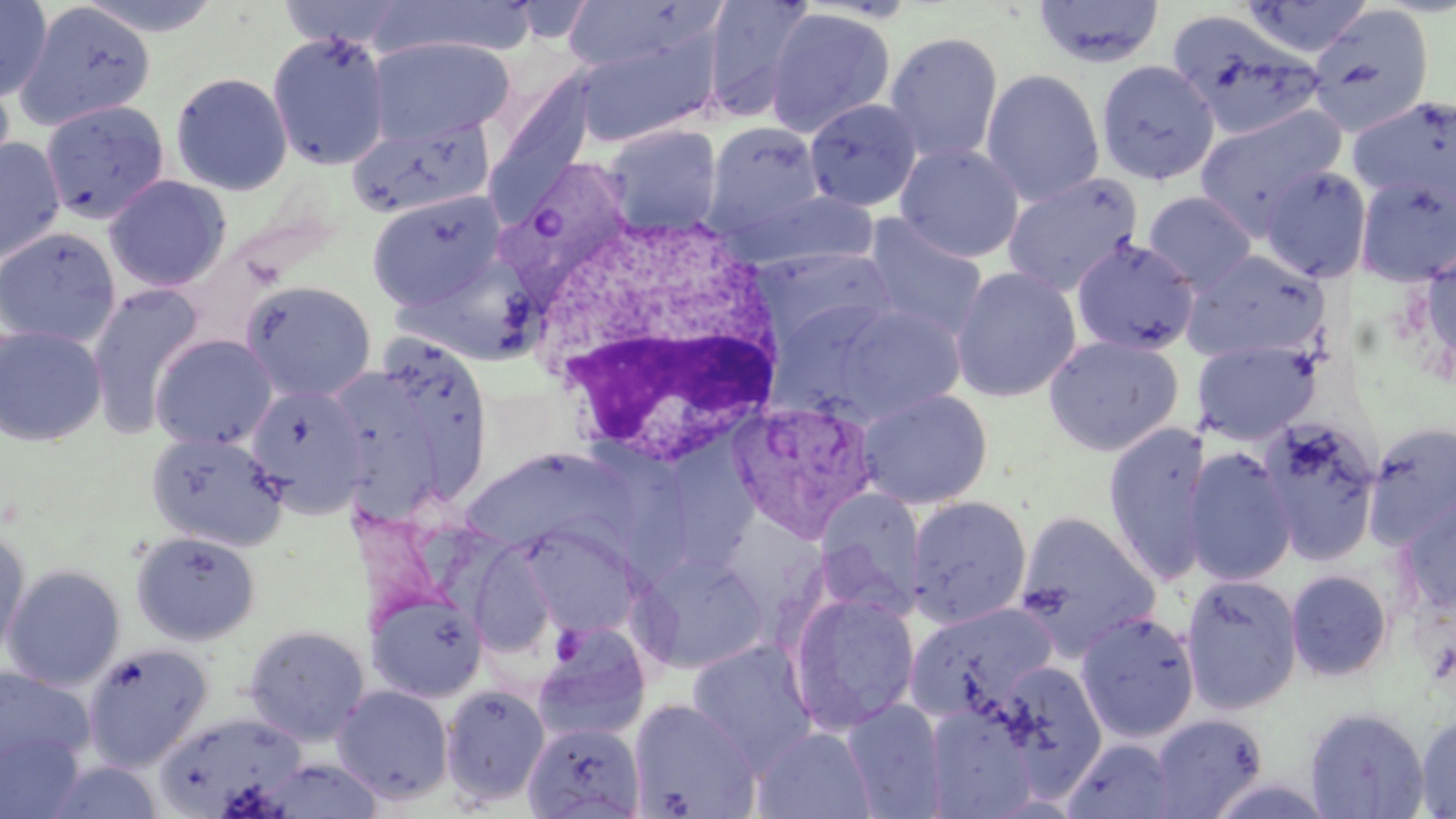

Summary:
  - Coordinate format: approximate bounding boxes as (x1,y1)-(x2,y2) corner pairs in pixels
  - White blood cell locations: (529,206)-(794,469)
  - Uninfected red blood cell locations: (0,0)-(53,102), (72,0)-(226,38), (276,0)-(410,51), (371,0)-(534,60), (701,0)-(816,122), (1031,0)-(1166,68), (1238,0)-(1375,58), (12,1)-(155,131), (557,1)-(715,73), (1307,4)-(1435,137), (764,7)-(896,138), (1166,9)-(1325,141), (572,27)-(722,148), (266,30)-(391,171), (883,31)-(1004,164), (366,37)-(515,144), (1095,59)-(1221,185), (0,65)-(16,187), (491,68)-(599,195), (981,69)-(1105,206), (170,72)-(293,196), (1348,94)-(1456,208), (804,98)-(922,212), (40,100)-(170,223), (1194,104)-(1347,237), (345,117)-(494,220), (704,122)-(826,236), (602,124)-(723,234), (0,137)-(66,264), (895,142)-(1025,262), (1259,165)-(1372,283), (1002,172)-(1143,296), (1355,174)-(1456,286), (104,175)-(232,292), (735,188)-(878,273), (366,191)-(507,310), (1142,191)-(1258,293), (861,215)-(989,342), (0,227)-(121,348), (1071,237)-(1200,356), (1418,246)-(1456,375), (751,247)-(899,355), (1182,249)-(1328,363), (948,266)-(1082,402), (242,281)-(377,402), (85,284)-(205,440), (810,302)-(968,423), (0,325)-(108,447), (150,334)-(277,450), (1042,334)-(1185,456), (365,339)-(497,504), (1193,339)-(1321,444), (246,383)-(369,516), (857,388)-(994,509), (1255,416)-(1382,564), (1361,420)-(1456,549), (1102,422)-(1213,585), (145,430)-(288,551), (583,438)-(689,578), (678,442)-(771,570), (1182,446)-(1297,586), (468,454)-(635,554), (813,488)-(926,620), (1398,493)-(1456,614), (907,495)-(1033,628), (1013,509)-(1162,660), (520,521)-(644,637), (0,529)-(31,663), (130,530)-(261,645), (463,535)-(558,658), (633,550)-(771,673), (2,565)-(125,691), (1286,569)-(1393,682), (1180,573)-(1303,715), (788,591)-(920,734), (368,592)-(488,702), (905,601)-(1058,725), (1075,610)-(1200,743), (243,624)-(370,746), (532,625)-(651,742), (686,639)-(817,770), (82,643)-(213,771), (995,660)-(1108,790), (0,666)-(95,771), (332,684)-(454,805), (439,684)-(551,807), (628,698)-(760,818), (841,699)-(947,818), (925,701)-(1041,817), (1304,706)-(1431,819), (154,711)-(307,816), (1415,711)-(1456,817), (1150,713)-(1267,817), (524,722)-(646,819), (752,726)-(876,818), (0,731)-(86,818), (1062,737)-(1176,819), (257,759)-(383,819), (43,760)-(164,819)
  - Plasmodium vivax-infected red blood cell locations: (490,160)-(639,304), (728,397)-(877,541)
  - Slide-level diagnosis: Plasmodium vivax
  - Image size: 1456×819 pixels
  - Modality: optical microscopy
  - Field of view: single
  - Preparation: thin blood smear
  - Stain: May-Grünwald-Giemsa
  - Magnification: 1000x